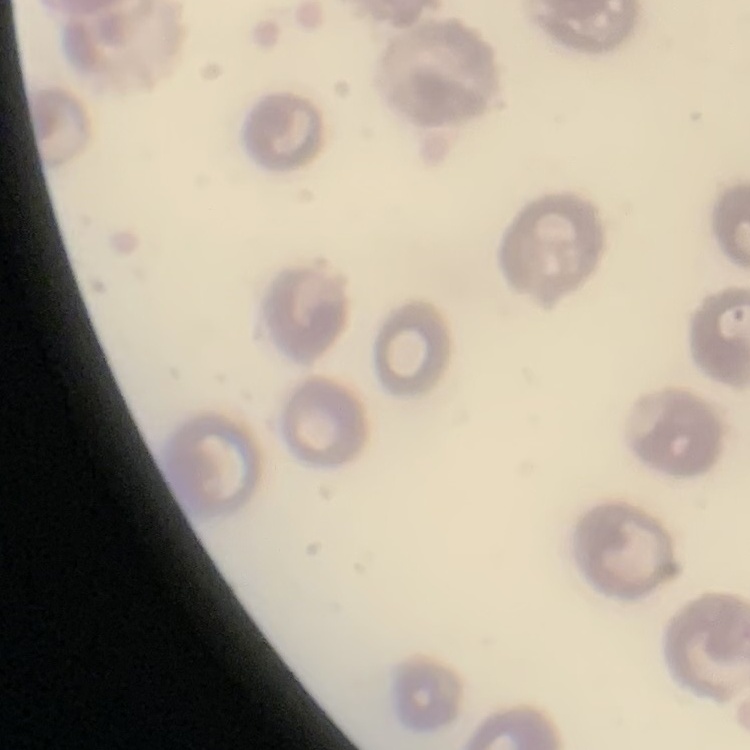

red blood cell morphology = no rouleaux formation
image type = one tile cut from a larger photomicrograph
preparation = thin peripheral smear
stain = Field's or Giemsa